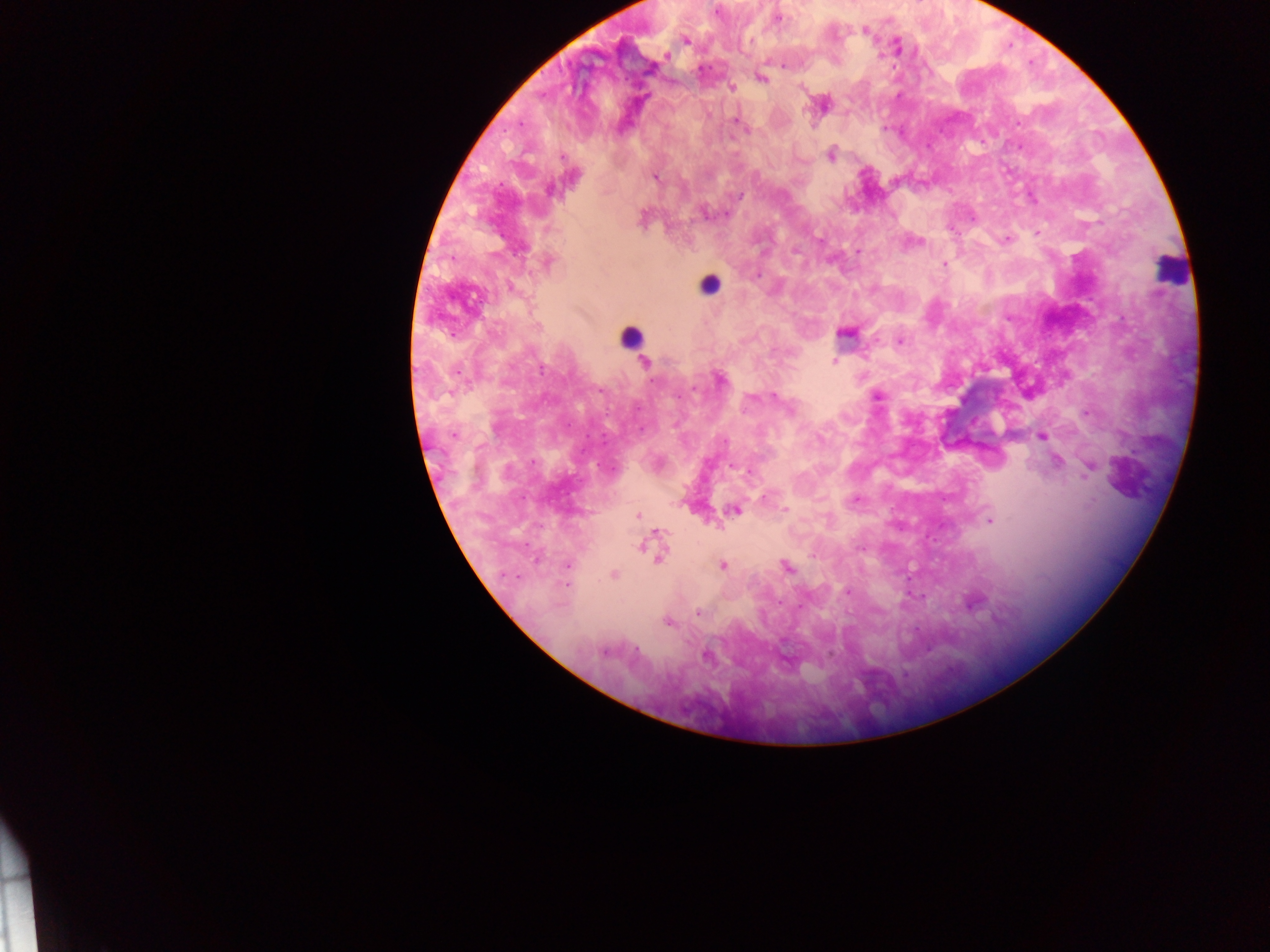
image size = 1270×952 pixels
leukocyte locations = approximate centers as (x, y) in pixels: (1169, 270), (710, 285), (631, 337)
field of view = single
preparation = thick blood film
capture = mobile-phone photograph through a microscope
Plasmodium parasite locations = approximate centers as (x, y) in pixels: (778, 18), (865, 30), (686, 40), (666, 55), (761, 79), (732, 87), (736, 121), (831, 156), (562, 157), (655, 177), (739, 197), (725, 214), (1037, 232), (819, 239), (1006, 239), (794, 251), (858, 251), (548, 262), (944, 264), (757, 275), (510, 286), (900, 341), (834, 361), (644, 362), (720, 379), (694, 390), (878, 397), (751, 398), (789, 408), (640, 429), (454, 434), (1041, 437), (726, 441), (1058, 461), (534, 462), (731, 465), (1088, 470), (750, 471), (763, 498), (855, 500), (784, 509), (734, 511), (637, 515), (989, 521), (658, 531), (640, 547), (859, 548), (813, 556), (660, 559), (567, 565), (723, 565), (787, 566), (614, 574), (566, 584), (848, 592), (780, 603), (698, 612), (668, 622), (604, 652), (706, 657)
country = Ghana